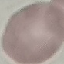
Malaria status: uninfected. Cell patch, automatically extracted from a larger field of view and resized to 64 × 64 pixels. Acquired by smartphone through the microscope eyepiece. Thin blood smear. Giemsa-stained preparation.